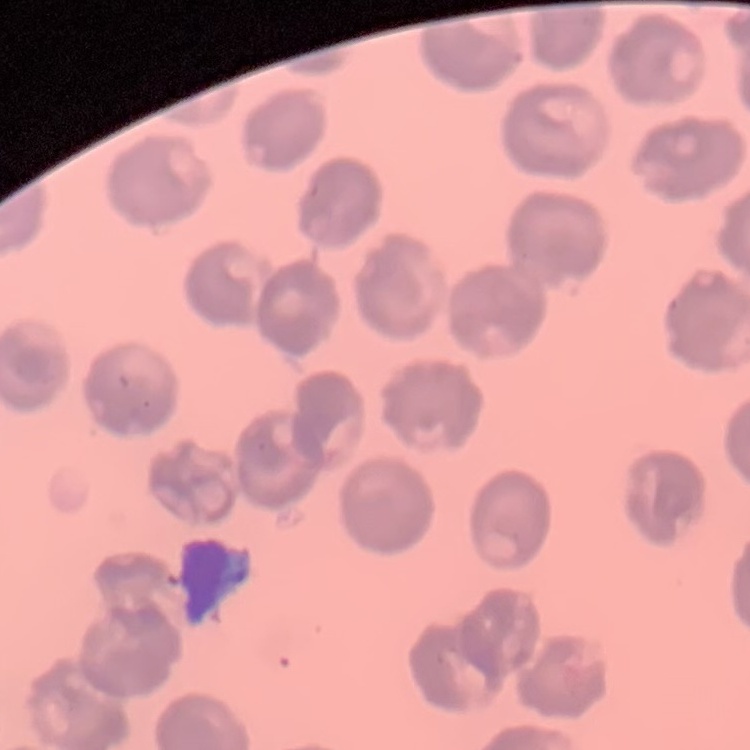
Summary:
  - Red blood cell morphology: no rouleaux formation
  - Image type: one tile cut from a larger photomicrograph
  - Stain: Field's or Giemsa
  - Preparation: thin peripheral smear